Assess this cell for malaria.
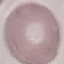
It is uninfected.

stain = Giemsa
image type = cell patch, automatically extracted from a larger field of view and resized to 64 × 64 pixels
capture = smartphone camera at the microscope eyepiece
preparation = thin blood smear